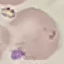 Result: malaria parasites detected. Thin blood film. Photographed with a smartphone camera at the microscope eyepiece. Automatically extracted cell patch, resized to 64 × 64 pixels. Giemsa-stained preparation.